State which parasite is depicted.
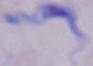
A trypanosome.

Summary:
  - Modality: micrograph
  - Magnification: 1000x